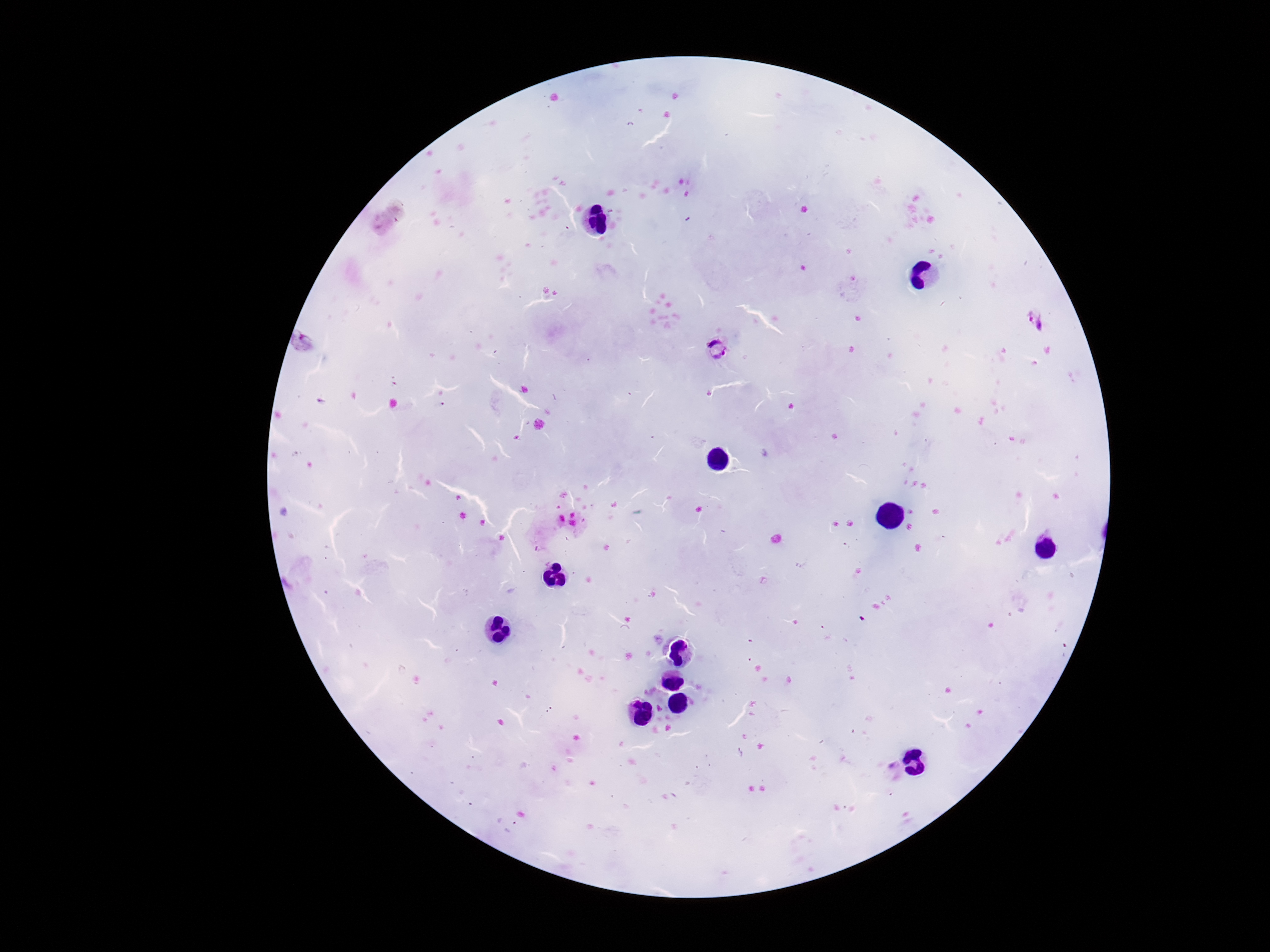

stain = Giemsa
magnification = 100x
Plasmodium parasite locations = approximate centers as (x, y) in pixels: (1036, 322), (305, 343), (718, 346)
capture = smartphone camera through the microscope eyepiece
patient malaria status = infected
preparation = thick blood film
field of view = single
image size = 1270×952 pixels